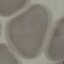

Malaria status: uninfected. Thin smear of blood. Acquired by smartphone through the microscope eyepiece. Giemsa stain. Automatically extracted cell patch, resized to 64 × 64 pixels.